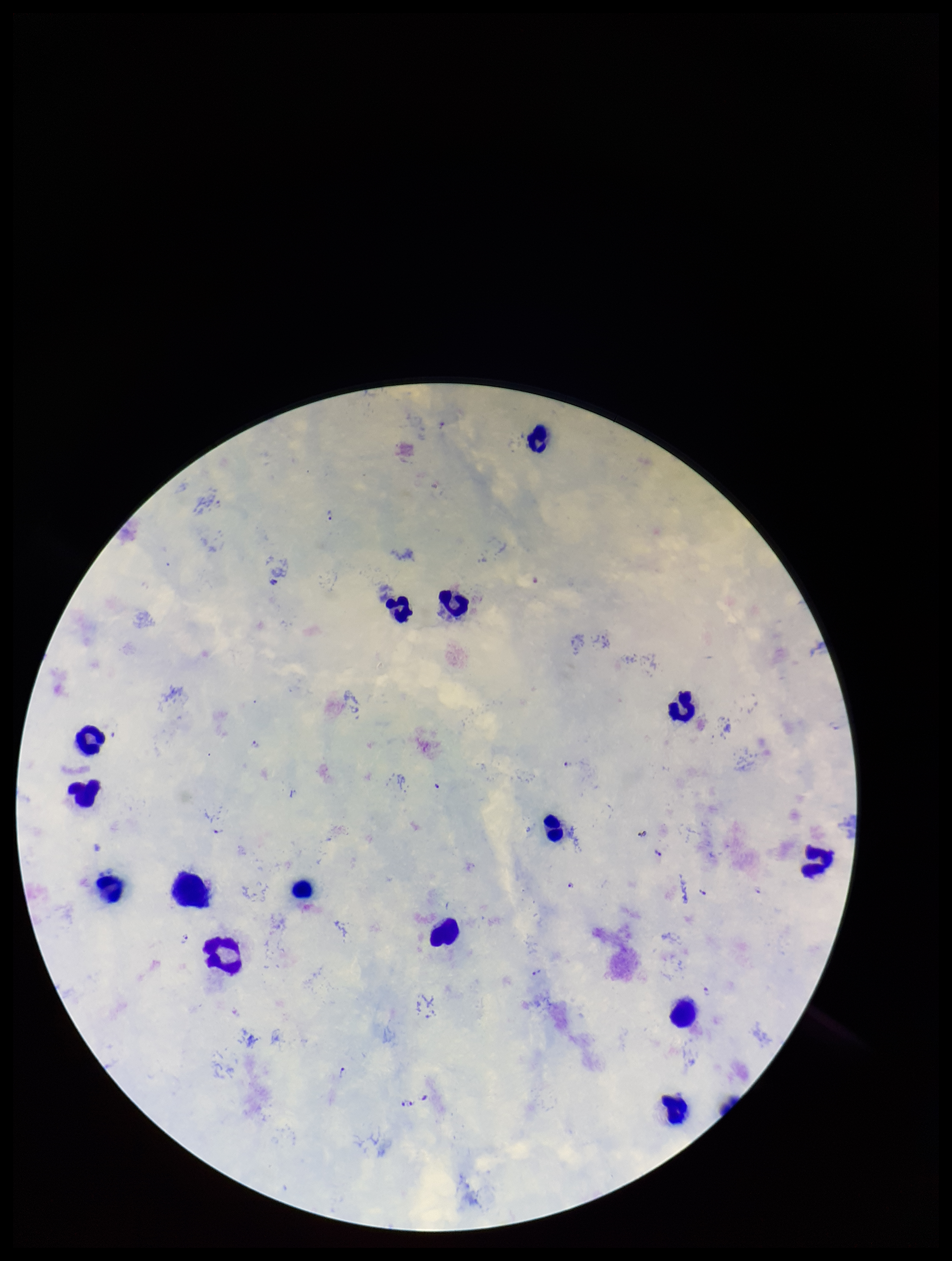

plasmodium_parasites: seen
patient_malaria_status: positive
species_reported_for_this_patient: Plasmodium falciparum
leukocyte_count: 15
stain: Giemsa
image_size: 952×1261 pixels
preparation: thick smear
field_of_view: single
capture: smartphone photograph through the microscope eyepiece
parasite_count: 18